Report the malaria status of this cell.
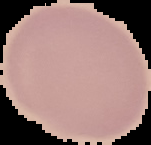
Uninfected.

Summary:
  - Image size: 151×145 pixels
  - Preparation: thin blood film
  - Image type: segmented cell region on a black background